State which cell type is depicted.
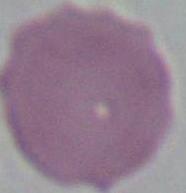
This is an erythrocyte.

Captured at 1000x magnification. Photomicrograph.